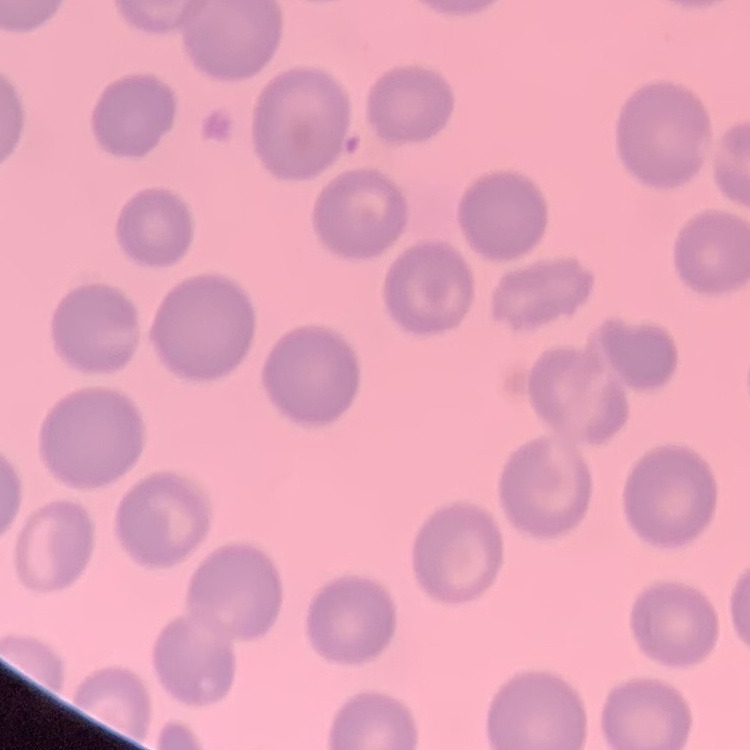
Summary:
  - Erythrocyte morphology: no rouleaux formation
  - Image type: one tile cut from a larger photomicrograph
  - Stain: Field's or Giemsa
  - Preparation: thin blood smear